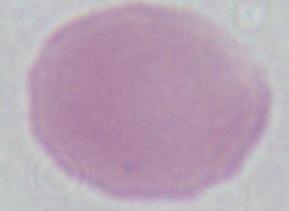
modality = micrograph
magnification = 1000x
identification = red blood cell